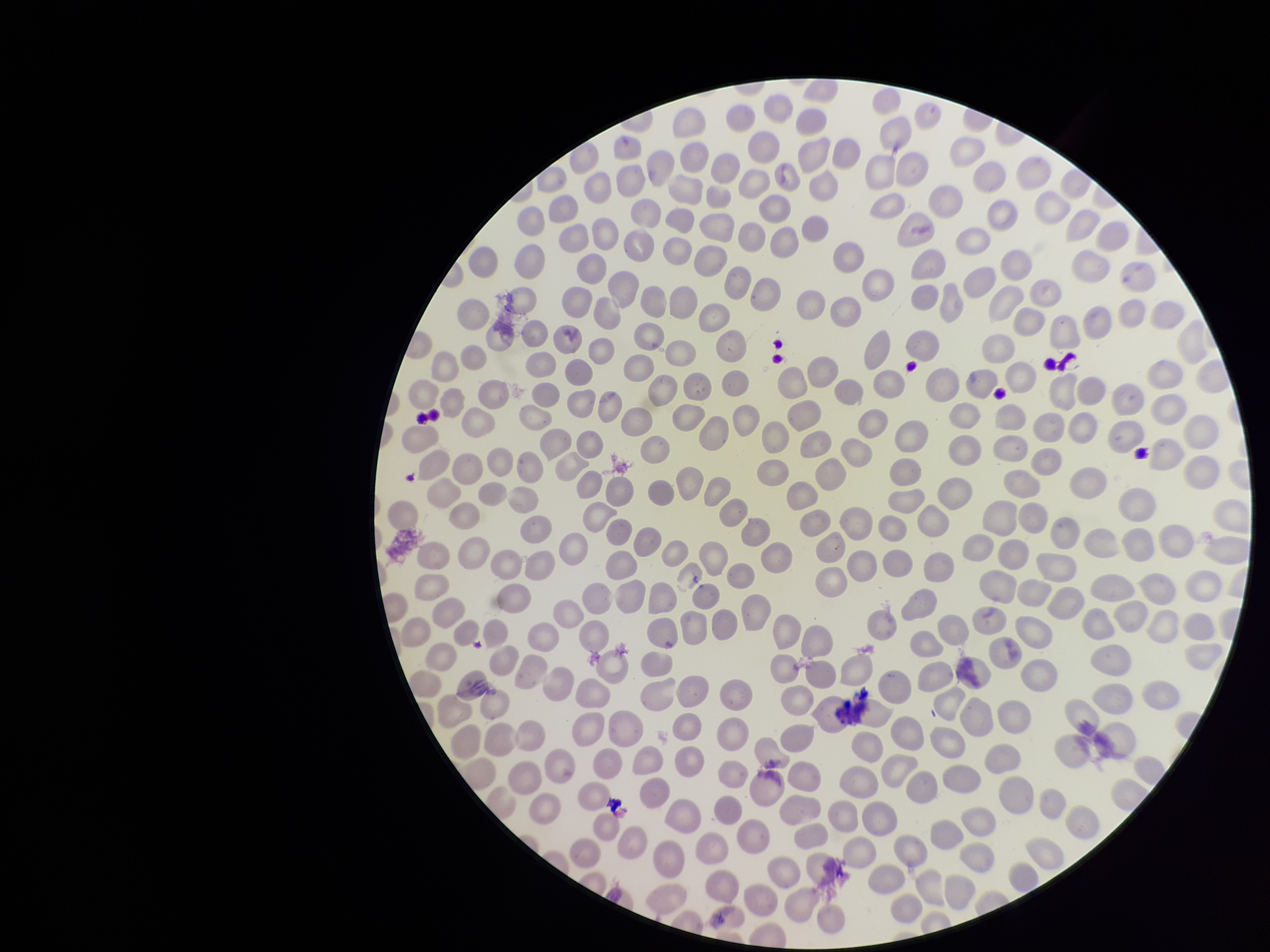

Preparation: thin smear. Single field of view. Image is 1270×952 pixels. Smartphone photograph taken through the eyepiece of a microscope. Red blood cell count: 277. Parasitized red blood cells: none seen. Stained with Giemsa. Species reported for this patient: Plasmodium vivax. Parasitized red blood cell count: 0. Patient malaria status: positive.